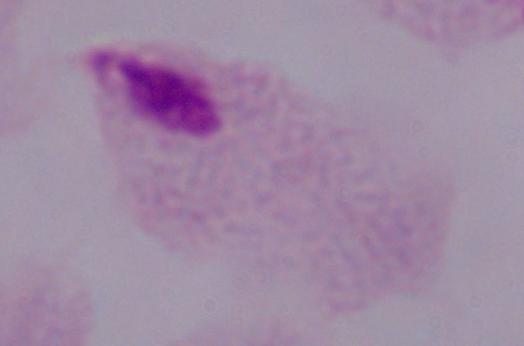
Captured at 1000x magnification. Micrograph. A trichomonad is shown.